Locate every leukocyte (white blood cell).
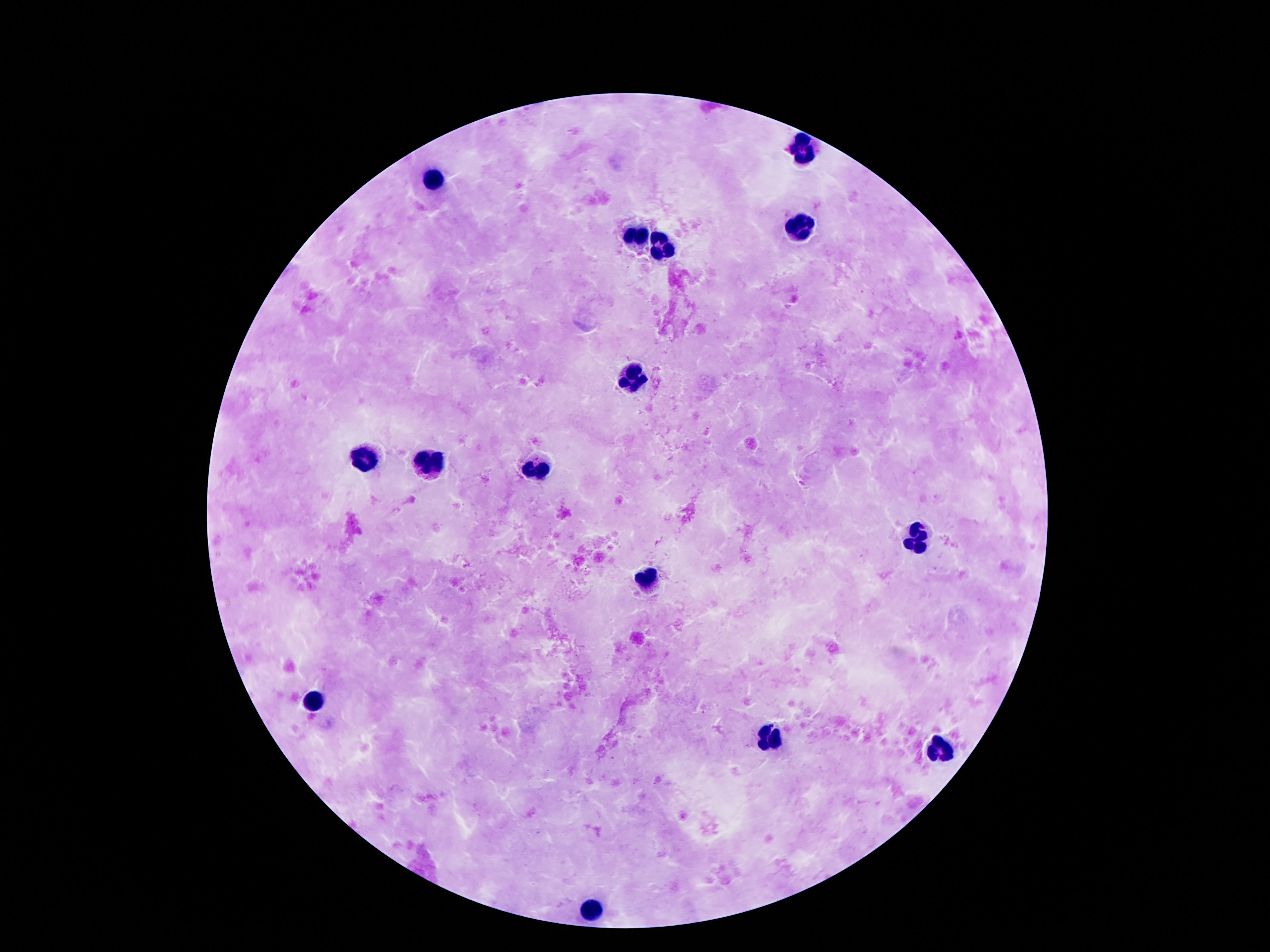
Approximate centers as {x, y} in pixels.
Leukocytes: {805, 151}, {434, 179}, {800, 229}, {635, 233}, {664, 244}, {634, 378}, {363, 458}, {434, 465}, {542, 467}, {917, 537}, {649, 576}, {314, 701}, {774, 736}, {938, 748}, {593, 906}.

Summary:
  - Image size: 1270×952 pixels
  - Preparation: thick blood smear
  - Field of view: single
  - Stain: Giemsa
  - Patient malaria status: negative
  - Capture: smartphone camera through the microscope eyepiece
  - Magnification: 100x